Mark where platelets are.
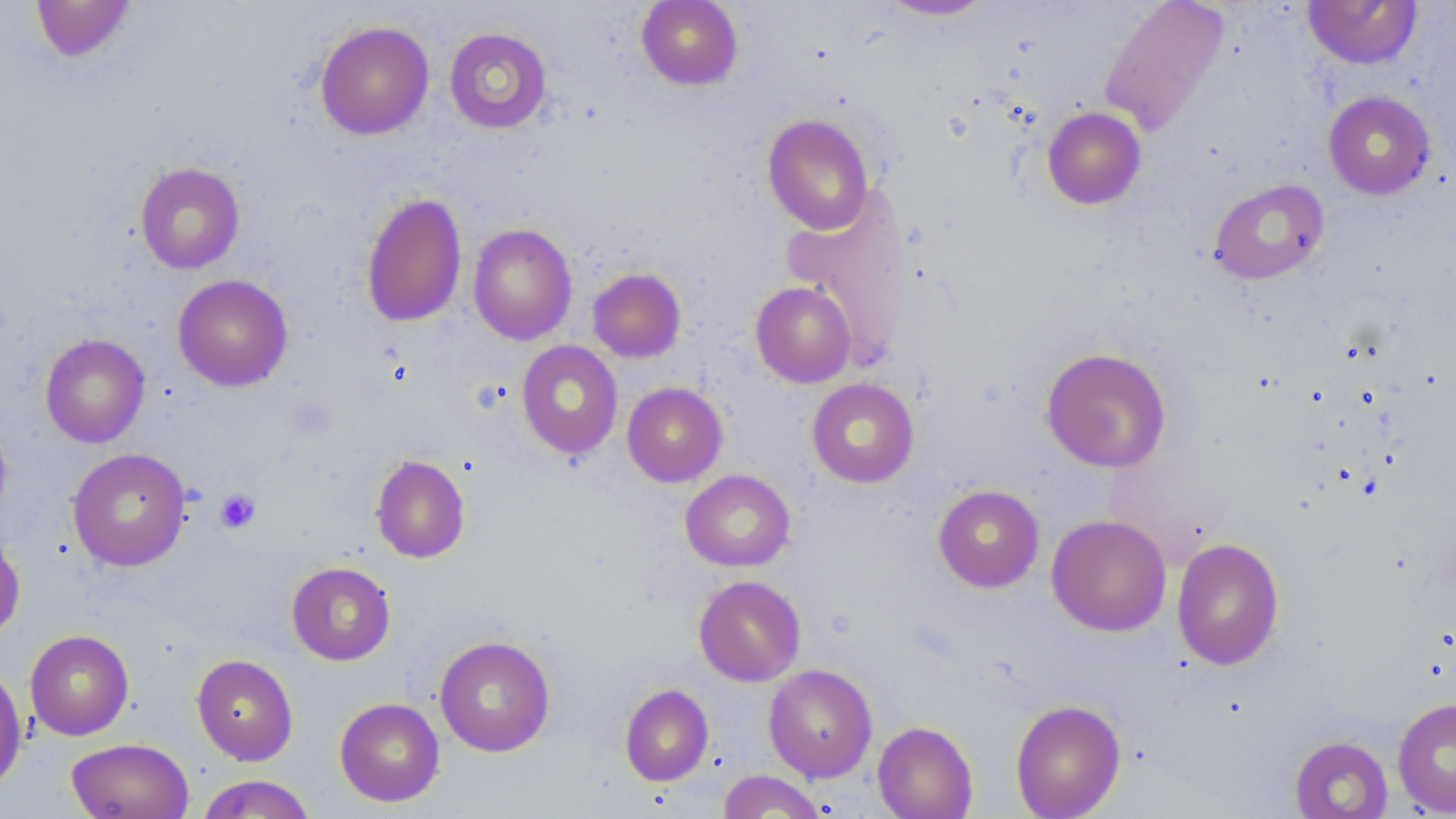

Approximate bounding boxes as (x1, y1, x2, y2) in pixels.
Platelets: (214, 488, 261, 534).

Uninfected red blood cell locations: (31, 0, 136, 62), (636, 0, 743, 90), (877, 0, 997, 21), (1099, 0, 1230, 136), (1303, 1, 1421, 69), (315, 20, 434, 139), (443, 26, 553, 133), (1323, 91, 1436, 199), (1042, 107, 1146, 209), (762, 113, 875, 235), (134, 161, 245, 274), (1208, 178, 1329, 284), (782, 189, 914, 370), (361, 191, 467, 328), (468, 223, 577, 345), (587, 267, 686, 363), (172, 274, 293, 391), (750, 281, 856, 387), (40, 333, 150, 448), (516, 340, 623, 459), (1040, 347, 1172, 472), (806, 378, 919, 488), (622, 382, 728, 487), (0, 413, 12, 526), (68, 448, 191, 571), (370, 454, 470, 563), (680, 469, 795, 572), (933, 484, 1045, 592), (1047, 514, 1171, 636), (0, 531, 25, 640), (1171, 537, 1285, 669), (286, 561, 396, 665), (693, 575, 806, 687), (25, 629, 134, 740), (434, 635, 556, 757), (191, 654, 299, 765), (763, 663, 878, 782), (0, 664, 27, 792), (620, 684, 713, 786), (1392, 696, 1456, 817), (334, 697, 445, 807), (1010, 699, 1125, 819), (873, 721, 978, 818), (1290, 735, 1393, 819), (66, 738, 194, 819), (717, 770, 828, 818), (196, 774, 317, 818). Slide-level diagnosis: no evidence of blood parasites. Captured at 1000x magnification. May-Grünwald-Giemsa-stained preparation. Thin blood smear. Light microscopy. Image is 1456×819 pixels. Single field of view.